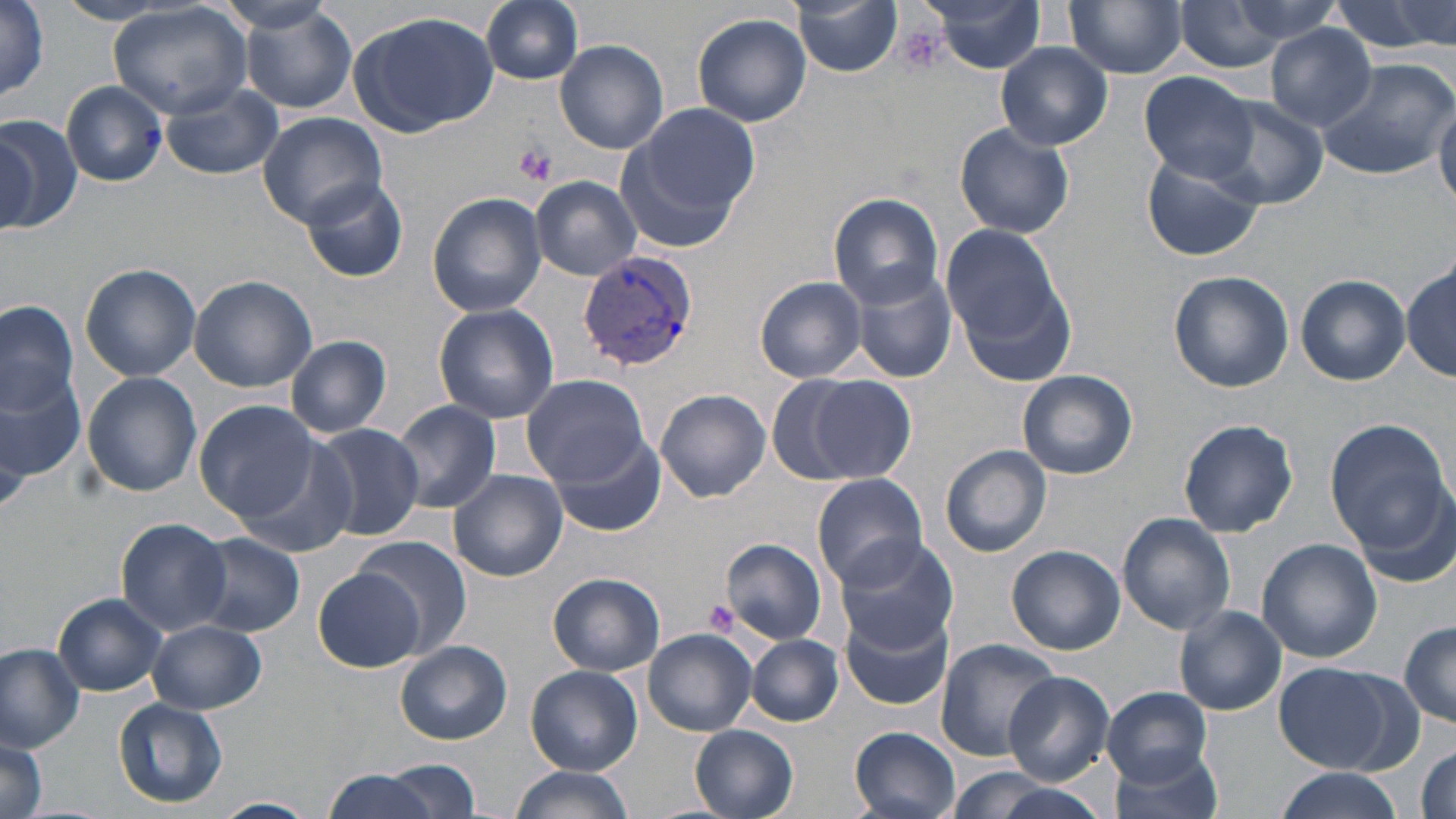 Approximate bounding boxes as named x1/y1/x2/y2 corners in pixels. Plasmodium vivax-infected red blood cell locations: (x1=577, y1=253, x2=699, y2=372). Platelet locations: (x1=896, y1=23, x2=948, y2=77), (x1=513, y1=143, x2=557, y2=186), (x1=704, y1=598, x2=738, y2=633). Uninfected red blood cell locations: (x1=481, y1=0, x2=584, y2=85), (x1=924, y1=0, x2=1048, y2=73), (x1=1206, y1=0, x2=1344, y2=53), (x1=1330, y1=0, x2=1454, y2=56), (x1=791, y1=1, x2=903, y2=76), (x1=1064, y1=1, x2=1187, y2=78), (x1=1169, y1=1, x2=1305, y2=74), (x1=54, y1=2, x2=179, y2=25), (x1=214, y1=2, x2=342, y2=38), (x1=0, y1=3, x2=51, y2=105), (x1=239, y1=3, x2=357, y2=113), (x1=109, y1=4, x2=252, y2=119), (x1=349, y1=10, x2=497, y2=136), (x1=692, y1=12, x2=813, y2=127), (x1=1266, y1=23, x2=1378, y2=128), (x1=555, y1=40, x2=669, y2=153), (x1=996, y1=42, x2=1114, y2=149), (x1=1316, y1=58, x2=1454, y2=181), (x1=1138, y1=72, x2=1259, y2=184), (x1=62, y1=80, x2=168, y2=186), (x1=161, y1=82, x2=284, y2=180), (x1=1207, y1=96, x2=1328, y2=212), (x1=1432, y1=100, x2=1456, y2=205), (x1=623, y1=102, x2=759, y2=237), (x1=256, y1=111, x2=388, y2=227), (x1=0, y1=114, x2=79, y2=235), (x1=954, y1=122, x2=1075, y2=239), (x1=1, y1=127, x2=40, y2=231), (x1=1142, y1=152, x2=1265, y2=262), (x1=531, y1=175, x2=642, y2=278), (x1=301, y1=177, x2=408, y2=283), (x1=426, y1=191, x2=547, y2=317), (x1=829, y1=192, x2=944, y2=307), (x1=942, y1=222, x2=1076, y2=378), (x1=1402, y1=261, x2=1454, y2=381), (x1=847, y1=262, x2=958, y2=382), (x1=81, y1=263, x2=200, y2=381), (x1=1168, y1=270, x2=1294, y2=392), (x1=188, y1=274, x2=316, y2=392), (x1=1296, y1=275, x2=1410, y2=385), (x1=755, y1=276, x2=867, y2=382), (x1=0, y1=300, x2=79, y2=425), (x1=433, y1=302, x2=559, y2=424), (x1=285, y1=335, x2=392, y2=437), (x1=0, y1=361, x2=86, y2=489), (x1=1017, y1=368, x2=1137, y2=479), (x1=82, y1=372, x2=202, y2=496), (x1=521, y1=372, x2=651, y2=486), (x1=800, y1=375, x2=917, y2=482), (x1=655, y1=390, x2=771, y2=503), (x1=194, y1=400, x2=324, y2=523), (x1=391, y1=401, x2=501, y2=512), (x1=1177, y1=420, x2=1299, y2=538), (x1=1326, y1=422, x2=1453, y2=554), (x1=308, y1=423, x2=424, y2=540), (x1=549, y1=433, x2=666, y2=539), (x1=240, y1=436, x2=360, y2=557), (x1=941, y1=444, x2=1053, y2=556), (x1=448, y1=470, x2=567, y2=581), (x1=812, y1=474, x2=929, y2=590), (x1=1356, y1=476, x2=1453, y2=589), (x1=1116, y1=513, x2=1236, y2=637), (x1=116, y1=518, x2=231, y2=636), (x1=188, y1=533, x2=306, y2=637), (x1=351, y1=537, x2=472, y2=659), (x1=721, y1=539, x2=827, y2=643), (x1=834, y1=539, x2=958, y2=653), (x1=1256, y1=539, x2=1383, y2=662), (x1=1005, y1=545, x2=1125, y2=655), (x1=315, y1=569, x2=422, y2=670), (x1=547, y1=573, x2=665, y2=676), (x1=53, y1=593, x2=168, y2=696), (x1=1174, y1=607, x2=1286, y2=715), (x1=841, y1=609, x2=954, y2=711), (x1=148, y1=619, x2=267, y2=713), (x1=1400, y1=619, x2=1456, y2=728), (x1=643, y1=628, x2=756, y2=735), (x1=749, y1=635, x2=842, y2=725), (x1=394, y1=639, x2=510, y2=745), (x1=935, y1=639, x2=1060, y2=763), (x1=0, y1=643, x2=85, y2=751), (x1=1271, y1=660, x2=1405, y2=773), (x1=527, y1=666, x2=642, y2=775), (x1=1005, y1=672, x2=1114, y2=784), (x1=1101, y1=686, x2=1213, y2=785), (x1=114, y1=698, x2=228, y2=808), (x1=690, y1=725, x2=799, y2=819), (x1=849, y1=727, x2=961, y2=819), (x1=0, y1=734, x2=49, y2=819), (x1=1414, y1=743, x2=1454, y2=819), (x1=1110, y1=745, x2=1228, y2=819), (x1=384, y1=758, x2=481, y2=817), (x1=317, y1=766, x2=447, y2=819), (x1=509, y1=766, x2=632, y2=819), (x1=935, y1=768, x2=1096, y2=819), (x1=1271, y1=769, x2=1398, y2=819), (x1=211, y1=797, x2=318, y2=818). Slide-level diagnosis: Plasmodium vivax. Captured at 1000x magnification. May-Grünwald-Giemsa stain. Thin blood film. Optical microscopy. One field of a larger specimen. Image is 1456×819 pixels.